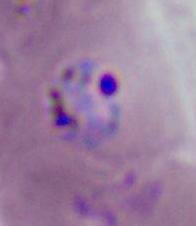

A Plasmodium parasite is seen. Photomicrograph. 400x or 1000x magnification.